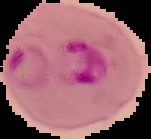
result = Plasmodium parasites detected
preparation = thin blood film
image size = 151×139 pixels
image type = cell region segmented out of the field of view; surrounding area masked to black